Outline each blood parasite and name the species.
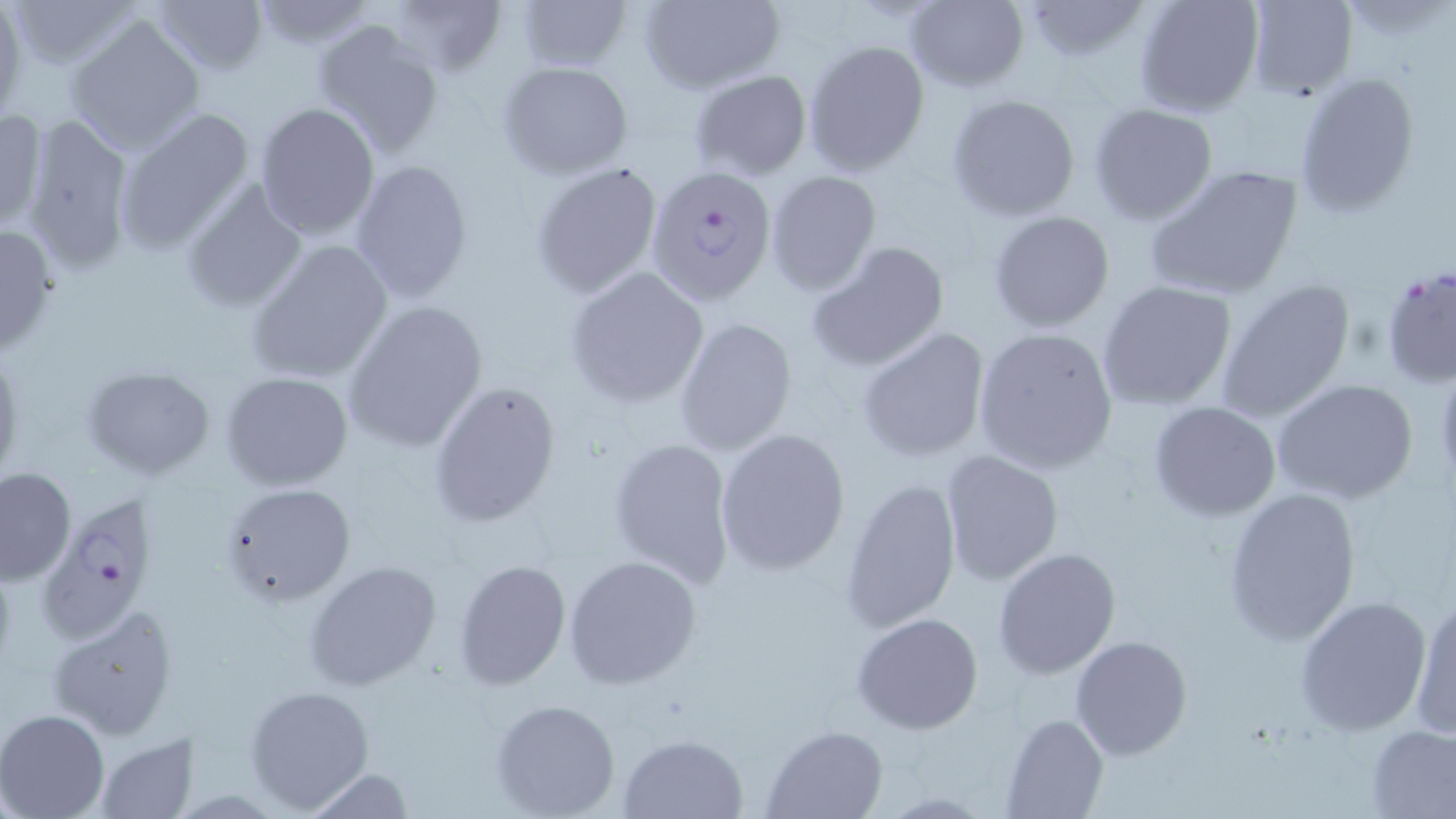
Approximate bounding boxes as named x1/y1/x2/y2 corners in pixels.
Plasmodium falciparum-infected red blood cells: (x1=644, y1=164, x2=775, y2=303), (x1=1381, y1=265, x2=1455, y2=390), (x1=40, y1=493, x2=159, y2=641).
No Plasmodium ovale, Plasmodium malariae, Plasmodium vivax, Babesia divergens, or Trypanosoma brucei observed.

slide-level diagnosis = Plasmodium falciparum
preparation = thin blood smear
uninfected red blood cell locations = approximate bounding boxes as named x1/y1/x2/y2 corners in pixels: (x1=9, y1=0, x2=143, y2=70), (x1=152, y1=0, x2=270, y2=76), (x1=247, y1=0, x2=375, y2=49), (x1=638, y1=0, x2=785, y2=93), (x1=902, y1=0, x2=1029, y2=91), (x1=1019, y1=0, x2=1148, y2=65), (x1=1134, y1=0, x2=1264, y2=116), (x1=1243, y1=0, x2=1357, y2=100), (x1=380, y1=1, x2=506, y2=79), (x1=513, y1=1, x2=634, y2=71), (x1=0, y1=4, x2=26, y2=118), (x1=66, y1=12, x2=207, y2=155), (x1=313, y1=19, x2=446, y2=158), (x1=802, y1=39, x2=929, y2=176), (x1=498, y1=60, x2=633, y2=178), (x1=1293, y1=68, x2=1423, y2=216), (x1=689, y1=70, x2=812, y2=180), (x1=945, y1=94, x2=1082, y2=222), (x1=254, y1=101, x2=381, y2=238), (x1=1088, y1=102, x2=1219, y2=225), (x1=0, y1=106, x2=47, y2=233), (x1=115, y1=107, x2=256, y2=253), (x1=20, y1=116, x2=139, y2=277), (x1=350, y1=159, x2=475, y2=302), (x1=529, y1=160, x2=664, y2=299), (x1=1142, y1=163, x2=1306, y2=301), (x1=766, y1=171, x2=881, y2=294), (x1=181, y1=181, x2=307, y2=310), (x1=987, y1=210, x2=1116, y2=333), (x1=0, y1=222, x2=59, y2=356), (x1=246, y1=239, x2=394, y2=385), (x1=806, y1=239, x2=953, y2=372), (x1=565, y1=266, x2=709, y2=406), (x1=1214, y1=277, x2=1357, y2=424), (x1=1097, y1=280, x2=1239, y2=411), (x1=343, y1=301, x2=488, y2=453), (x1=674, y1=315, x2=800, y2=456), (x1=973, y1=326, x2=1118, y2=473), (x1=857, y1=328, x2=991, y2=464), (x1=0, y1=347, x2=24, y2=486), (x1=78, y1=363, x2=217, y2=480), (x1=221, y1=372, x2=354, y2=490), (x1=1271, y1=379, x2=1420, y2=505), (x1=429, y1=380, x2=562, y2=528), (x1=1150, y1=402, x2=1281, y2=520), (x1=714, y1=428, x2=851, y2=576), (x1=607, y1=435, x2=736, y2=590), (x1=940, y1=449, x2=1063, y2=586), (x1=0, y1=466, x2=77, y2=585), (x1=840, y1=476, x2=964, y2=634), (x1=217, y1=483, x2=358, y2=607), (x1=1222, y1=486, x2=1362, y2=646), (x1=993, y1=548, x2=1121, y2=680), (x1=564, y1=555, x2=703, y2=690), (x1=453, y1=558, x2=572, y2=690), (x1=304, y1=561, x2=444, y2=693), (x1=1407, y1=592, x2=1456, y2=742), (x1=1294, y1=594, x2=1433, y2=734), (x1=45, y1=603, x2=179, y2=739), (x1=851, y1=613, x2=984, y2=734), (x1=1069, y1=634, x2=1193, y2=760), (x1=245, y1=684, x2=375, y2=814), (x1=489, y1=698, x2=622, y2=818), (x1=0, y1=710, x2=108, y2=819), (x1=1001, y1=712, x2=1107, y2=819), (x1=1365, y1=724, x2=1455, y2=818), (x1=760, y1=725, x2=887, y2=818), (x1=94, y1=733, x2=198, y2=818), (x1=617, y1=733, x2=747, y2=818), (x1=299, y1=767, x2=418, y2=818)
stain = May-Grünwald-Giemsa
field of view = single
modality = light microscopy
magnification = 1000x
image size = 1456×819 pixels